Locate every Plasmodium parasite.
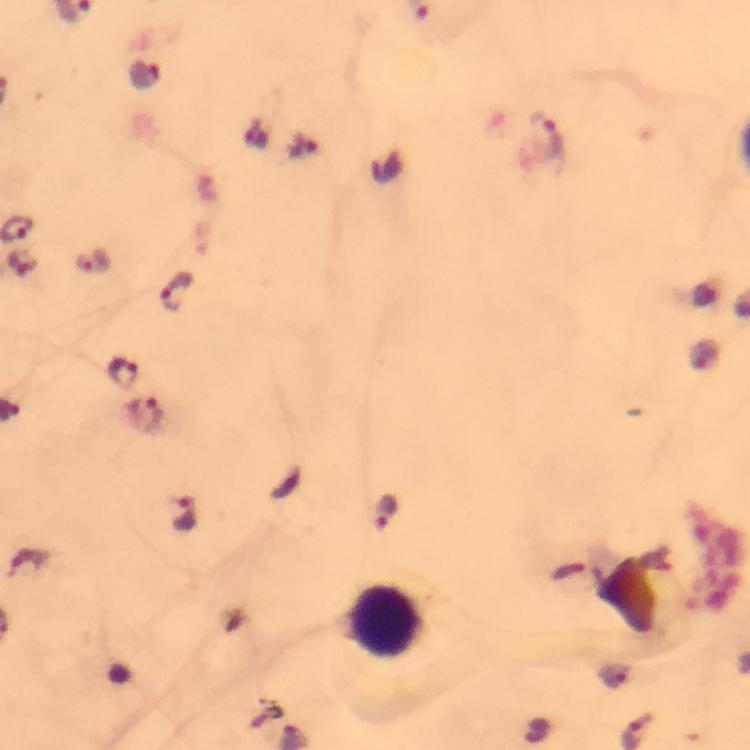
Approximate centers as [x, y] in pixels.
Plasmodium parasites: [144, 73], [548, 137], [93, 261], [173, 292], [122, 372], [144, 415], [383, 512], [185, 518].

Summary:
  - Leukocyte locations: [384, 622]
  - Magnification: 100x
  - Preparation: thick blood smear
  - Capture: smartphone mounted on the microscope
  - Immersion oil: applied
  - Cropped from: a single field of view
  - Image size: 750×750 pixels
  - Stain: Giemsa
  - Context: from a diagnostic examination for malaria